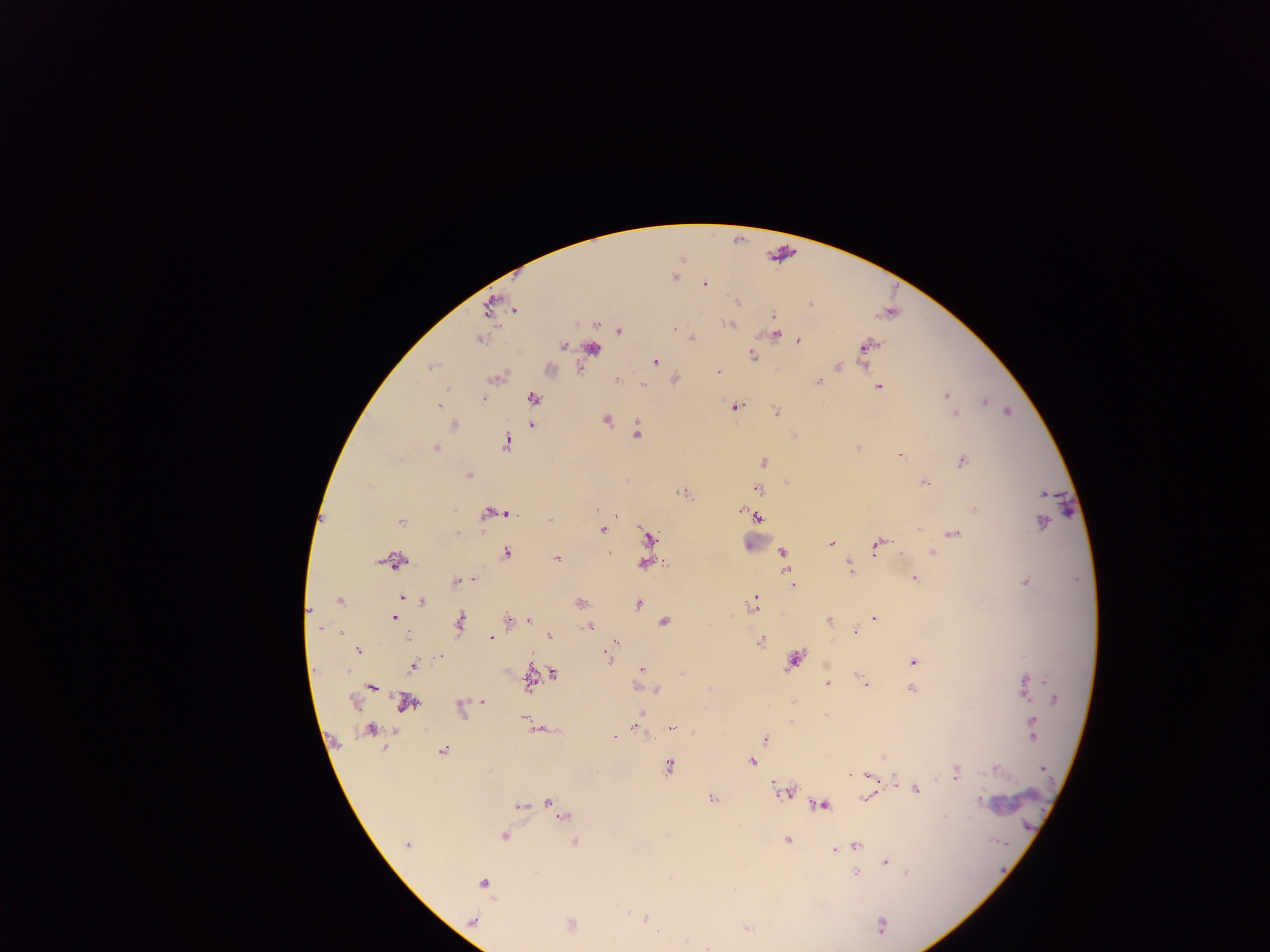

preparation = thick blood smear
field of view = single
country = Ghana
image size = 1270×952 pixels
Plasmodium parasite locations = approximate centers as {x, y} in pixels: {675, 277}, {705, 284}, {738, 301}, {810, 304}, {490, 306}, {515, 310}, {773, 316}, {731, 325}, {674, 328}, {619, 331}, {774, 334}, {692, 338}, {798, 340}, {478, 341}, {564, 346}, {864, 346}, {593, 349}, {752, 355}, {655, 362}, {432, 365}, {838, 366}, {549, 369}, {718, 372}, {617, 380}, {819, 381}, {641, 385}, {878, 387}, {446, 389}, {945, 395}, {533, 398}, {483, 399}, {984, 401}, {438, 405}, {735, 406}, {1007, 411}, {776, 412}, {955, 414}, {607, 420}, {454, 425}, {532, 425}, {637, 433}, {507, 443}, {858, 447}, {435, 448}, {900, 455}, {764, 462}, {962, 462}, {468, 476}, {924, 483}, {757, 489}, {681, 493}, {1044, 493}, {597, 509}, {974, 509}, {741, 511}, {500, 513}, {488, 514}, {615, 514}, {758, 516}, {550, 520}, {400, 522}, {1043, 522}, {603, 530}, {457, 532}, {953, 534}, {648, 538}, {831, 544}, {878, 545}, {783, 552}, {932, 552}, {507, 553}, {609, 553}, {557, 558}, {397, 561}, {644, 564}, {850, 568}, {914, 578}, {473, 579}, {456, 582}, {1026, 582}, {792, 584}, {401, 596}, {339, 602}, {422, 602}, {581, 602}, {754, 603}, {637, 604}, {308, 612}, {393, 618}, {875, 618}, {508, 620}, {528, 620}, {828, 621}, {460, 622}, {664, 622}, {587, 626}, {319, 628}, {855, 632}, {340, 633}, {549, 635}, {408, 636}, {491, 638}, {761, 641}, {615, 642}, {358, 651}, {610, 652}, {440, 657}, {607, 657}, {793, 661}, {913, 662}, {412, 666}, {641, 669}, {553, 673}, {530, 682}, {827, 683}, {1026, 683}, {865, 684}, {371, 688}, {911, 689}, {656, 690}, {1055, 699}, {352, 702}, {406, 703}, {483, 703}, {461, 709}, {641, 713}, {826, 715}, {635, 726}, {1032, 726}, {671, 728}, {369, 730}, {614, 736}, {764, 738}, {442, 751}, {752, 762}, {668, 766}, {1044, 769}, {995, 770}, {850, 774}, {955, 774}, {870, 776}, {895, 782}, {916, 790}, {784, 792}, {866, 797}, {712, 799}, {979, 801}, {549, 802}, {822, 805}, {520, 806}, {557, 807}, {564, 814}, {945, 817}, {504, 836}, {788, 840}, {574, 842}, {407, 845}, {855, 845}, {835, 849}, {886, 862}, {855, 874}, {907, 874}, {670, 878}, {483, 883}, {646, 918}, {474, 920}, {570, 924}, {881, 925}, {748, 929}, {658, 932}, {708, 948}
leukocyte locations = approximate centers as {x, y} in pixels: {756, 539}
capture = mobile-phone photograph through a microscope